Assess this cell for malaria.
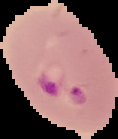
Parasitized.

Image is 118×139 pixels. From a thin blood smear. Segmented cell region on a black background.